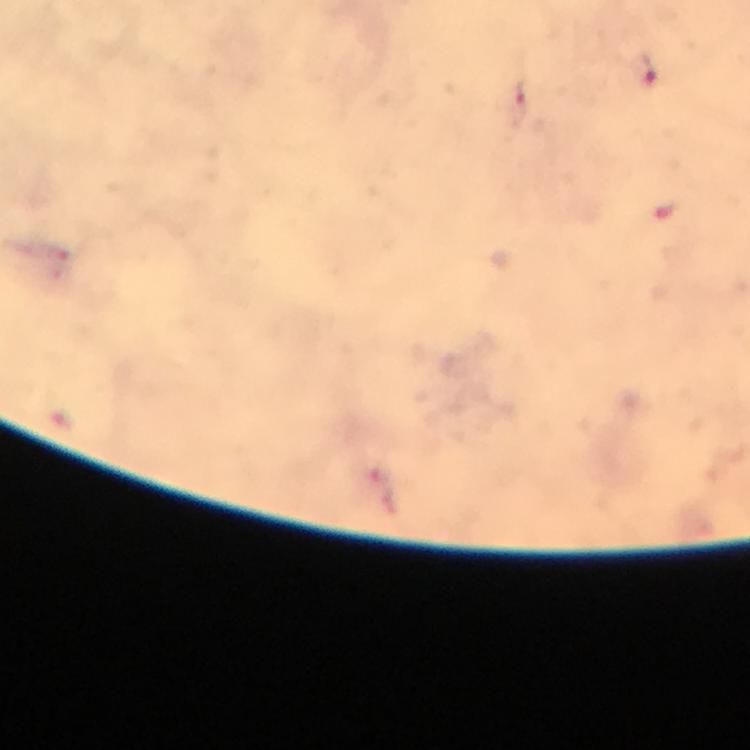 Approximate centers as {x, y} in pixels. Malaria parasite locations: {643, 71}, {520, 99}. From a diagnostic examination for malaria. Photographed through the microscope with a smartphone camera. Giemsa stain. A crop from one field of view. Immersion oil was used. Thick smear. 100x magnification. Image is 750×750 pixels.